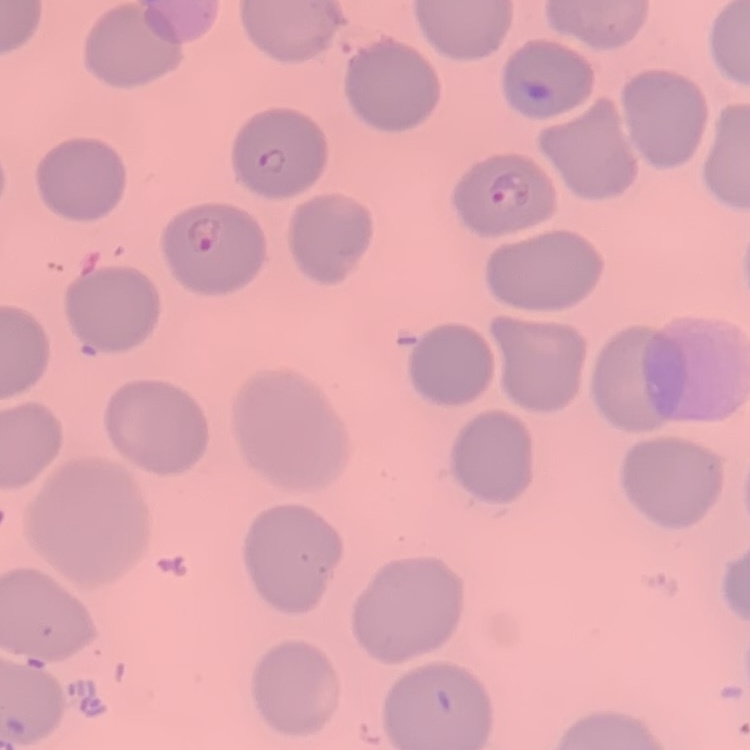
red blood cell morphology = no rouleaux formation
preparation = thin blood smear
image type = one tile cut from a larger photomicrograph
stain = Field's or Giemsa